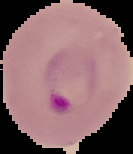
The area outside the segmented cell region is set to black. Result: Plasmodium parasites detected. Image is 133×154 pixels. From a thin blood film.